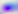

magnification: 400x
modality: photomicrograph
identification: Toxoplasma gondii